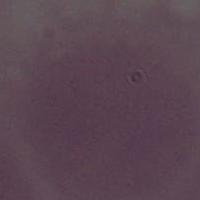
modality = micrograph
identification = erythrocyte
magnification = 1000x